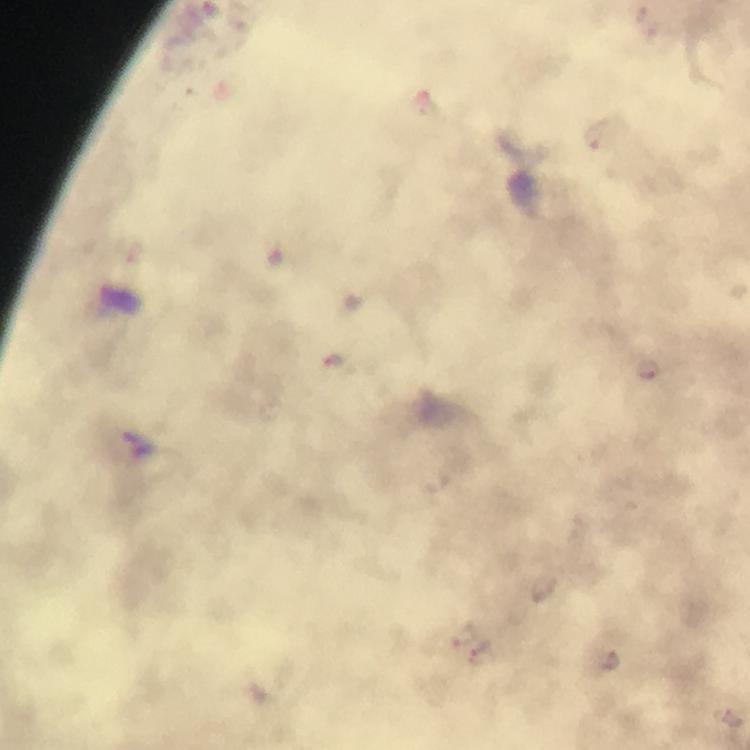
Approximate object centers, in pixels from the top-left corner.
Summary:
  - Malaria parasite locations: (x=464, y=633), (x=480, y=655), (x=610, y=663)
  - Image size: 750×750 pixels
  - Context: from a malaria diagnostic workup
  - Cropped from: a single field of view
  - Capture: smartphone photograph through a microscope
  - Magnification: 100x
  - Immersion oil: applied
  - Stain: Giemsa
  - Preparation: thick blood film